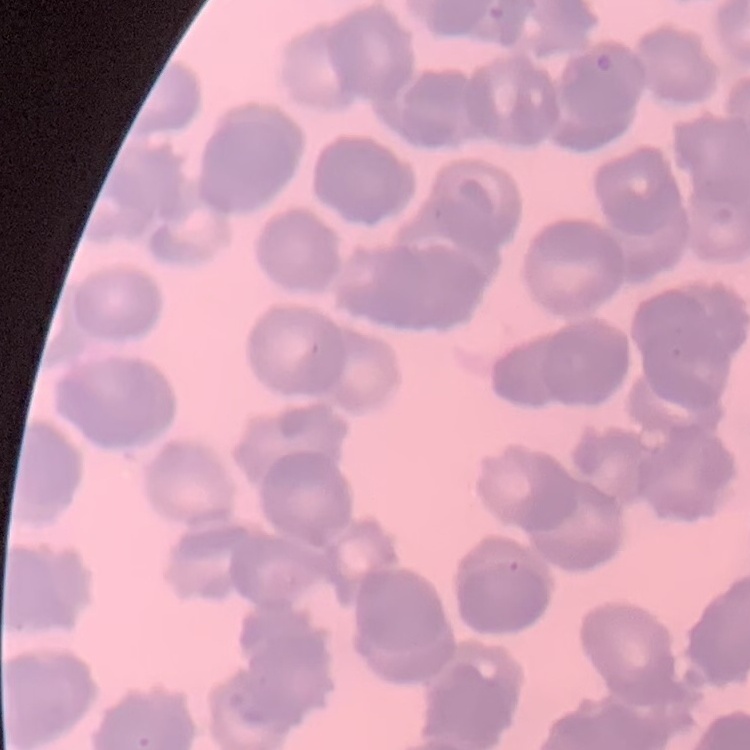
Summary:
  - Red blood cell morphology: rouleaux formation
  - Preparation: thin blood smear
  - Image type: square crop of a larger photomicrograph
  - Stain: Field's or Giemsa